Report the malaria status of this cell.
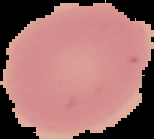
Uninfected.

Image is 154×139 pixels. From a thin blood film. Cell region segmented out of the field of view; the surrounding area is masked to black.